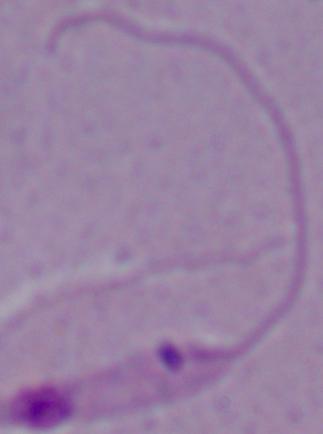

Summary:
  - Identification: Leishmania
  - Magnification: 1000x
  - Modality: micrograph